Give the position of every Plasmodium parasite visible.
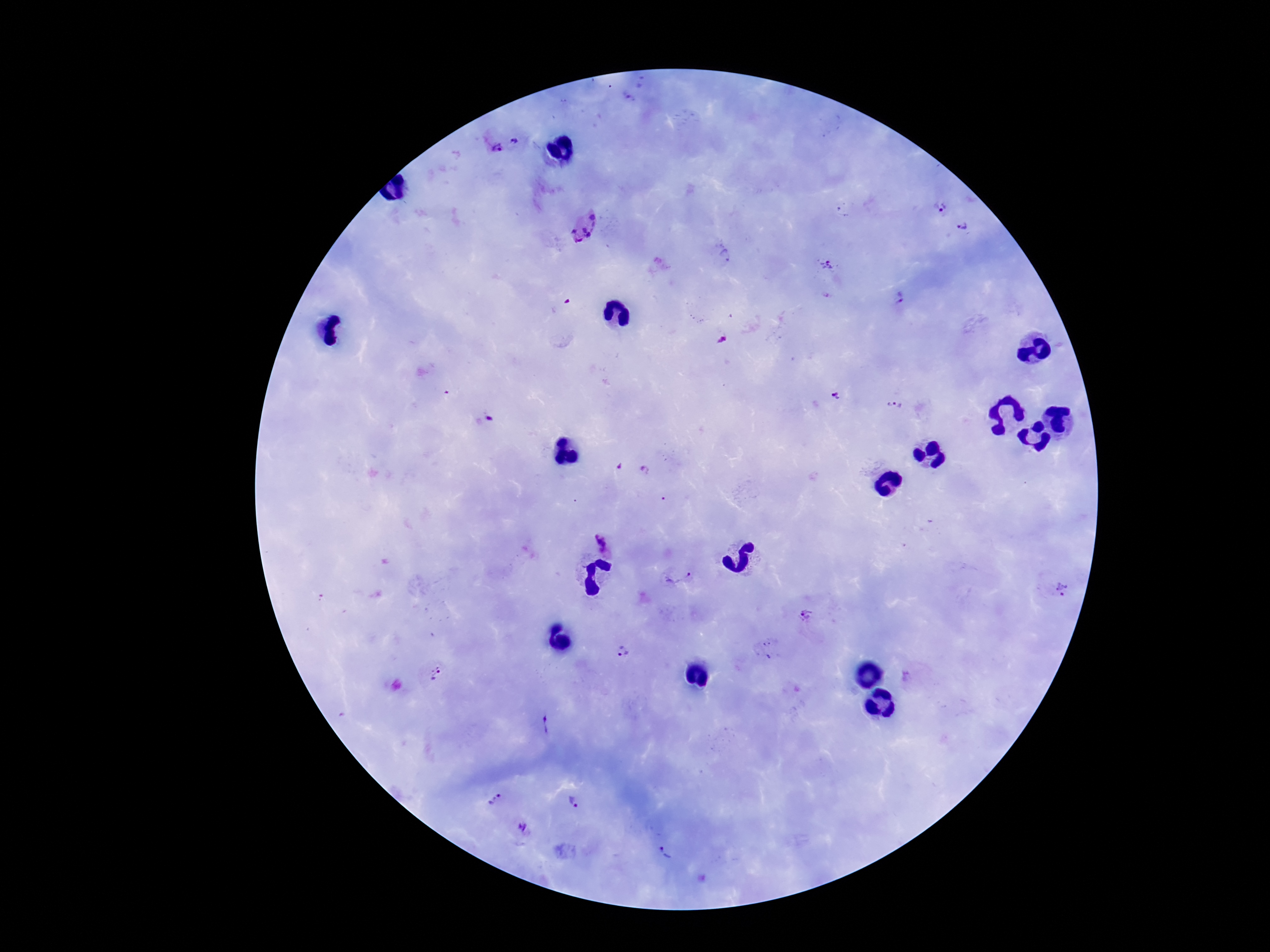

Approximate centers as {x, y} in pixels.
Plasmodium parasites: {518, 141}, {495, 148}, {941, 208}, {580, 226}, {964, 227}, {724, 258}, {828, 265}, {901, 297}, {837, 396}, {895, 403}, {489, 419}, {617, 467}, {645, 471}, {602, 543}, {678, 570}, {1057, 591}, {803, 615}, {621, 649}, {435, 674}, {549, 722}, {489, 796}, {580, 806}, {523, 825}, {670, 847}.

Summary:
  - Magnification: 100x
  - Capture: smartphone camera through the microscope eyepiece
  - Preparation: thick blood film
  - Patient malaria status: positive
  - Image size: 1270×952 pixels
  - Stain: Giemsa
  - Field of view: one from this slide